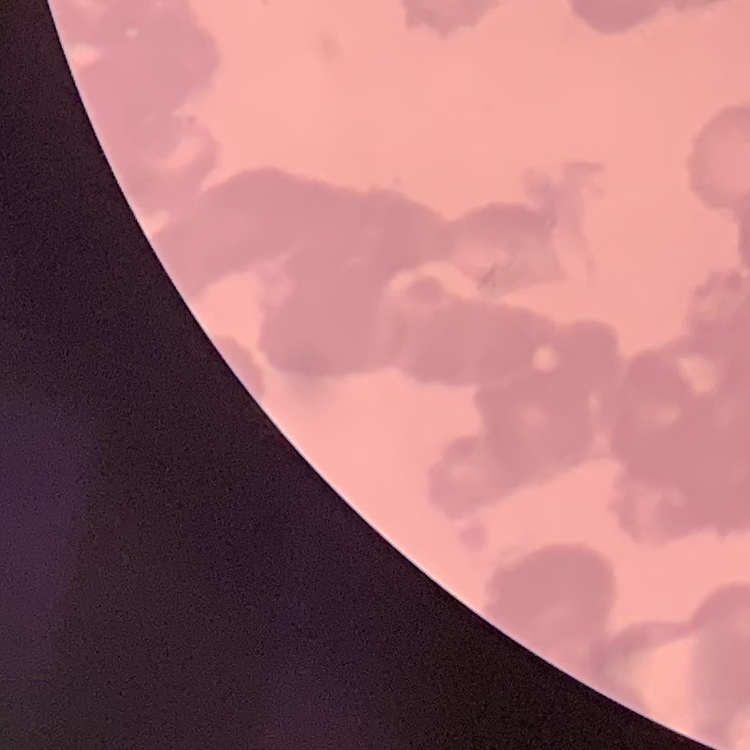 The erythrocytes show rouleaux formation. Thin blood film. Stained with either Field's or Giemsa. One tile cut from a larger photomicrograph.